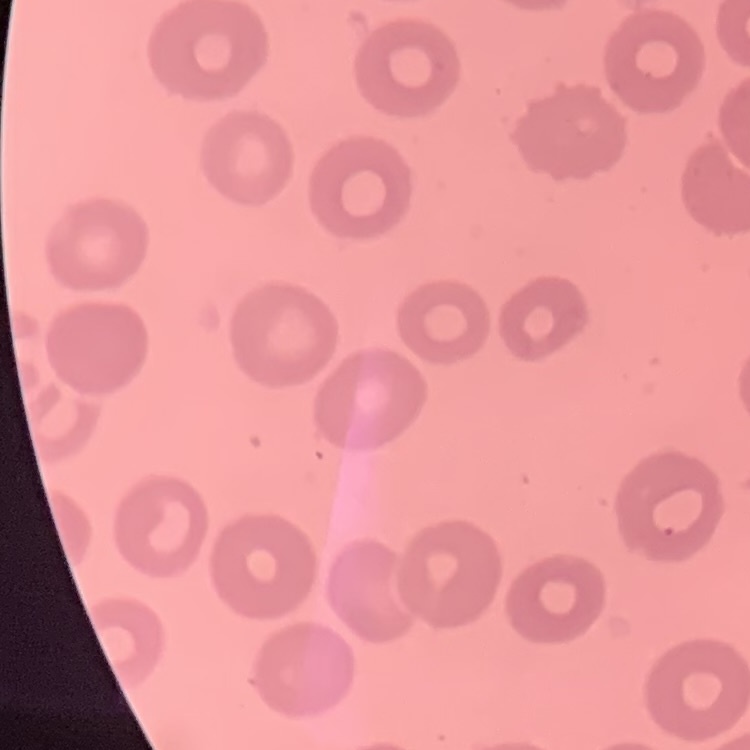
{
  "erythrocyte_morphology": "no rouleaux formation",
  "preparation": "thin blood film",
  "image_type": "square crop of a larger photomicrograph",
  "stain": "Field's or Giemsa"
}